Point out every Plasmodium parasite.
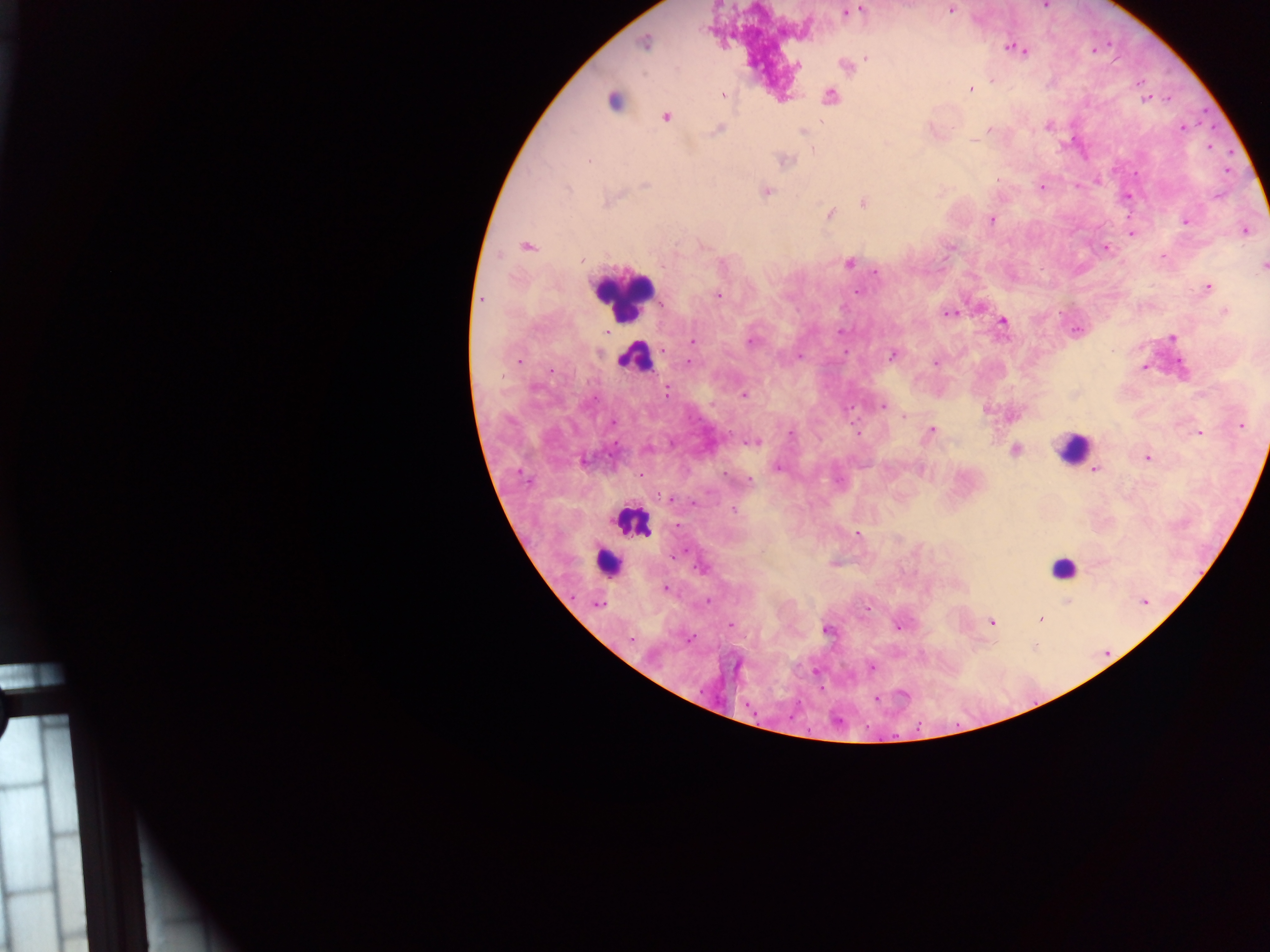
Approximate centers as {x, y} in pixels.
Plasmodium parasites: {1044, 6}, {951, 9}, {859, 10}, {846, 12}, {644, 43}, {1015, 48}, {866, 58}, {797, 65}, {970, 89}, {723, 95}, {830, 97}, {614, 100}, {1145, 100}, {665, 117}, {1183, 128}, {717, 130}, {989, 130}, {803, 133}, {589, 160}, {786, 161}, {646, 183}, {1042, 187}, {568, 189}, {766, 191}, {863, 203}, {830, 213}, {991, 220}, {1186, 222}, {1244, 230}, {1131, 232}, {527, 246}, {951, 247}, {1106, 249}, {581, 261}, {849, 263}, {722, 264}, {1262, 267}, {876, 272}, {1207, 288}, {857, 291}, {718, 295}, {482, 300}, {1226, 312}, {949, 314}, {1003, 322}, {1077, 330}, {841, 332}, {1172, 338}, {693, 341}, {751, 341}, {664, 351}, {598, 353}, {892, 354}, {799, 356}, {518, 361}, {690, 363}, {935, 363}, {1146, 367}, {552, 371}, {666, 391}, {744, 395}, {882, 406}, {904, 416}, {1242, 426}, {931, 430}, {1198, 433}, {792, 435}, {754, 442}, {1015, 450}, {1147, 458}, {584, 460}, {778, 467}, {1095, 469}, {666, 498}, {734, 510}, {857, 533}, {701, 568}, {665, 588}, {1145, 601}, {599, 604}, {1040, 618}, {991, 621}, {731, 625}, {900, 626}, {826, 630}, {689, 639}, {631, 640}, {871, 667}, {876, 698}.

Summary:
  - Leukocyte locations: {622, 295}, {634, 358}, {1072, 448}, {635, 521}, {607, 563}, {1063, 566}
  - Preparation: thick blood smear
  - Image size: 1270×952 pixels
  - Field of view: single
  - Capture: mobile-phone photograph through a microscope
  - Country: Ghana